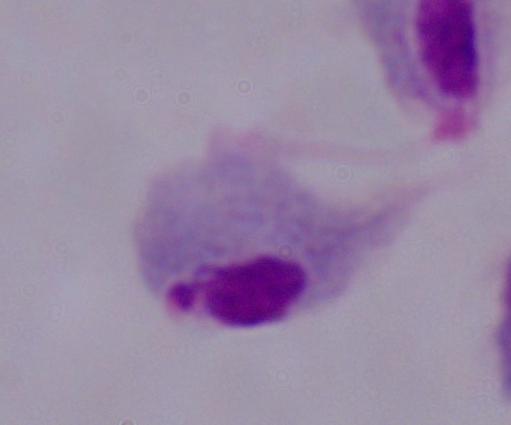 Micrograph. A trichomonad is seen. Captured at 1000x magnification.